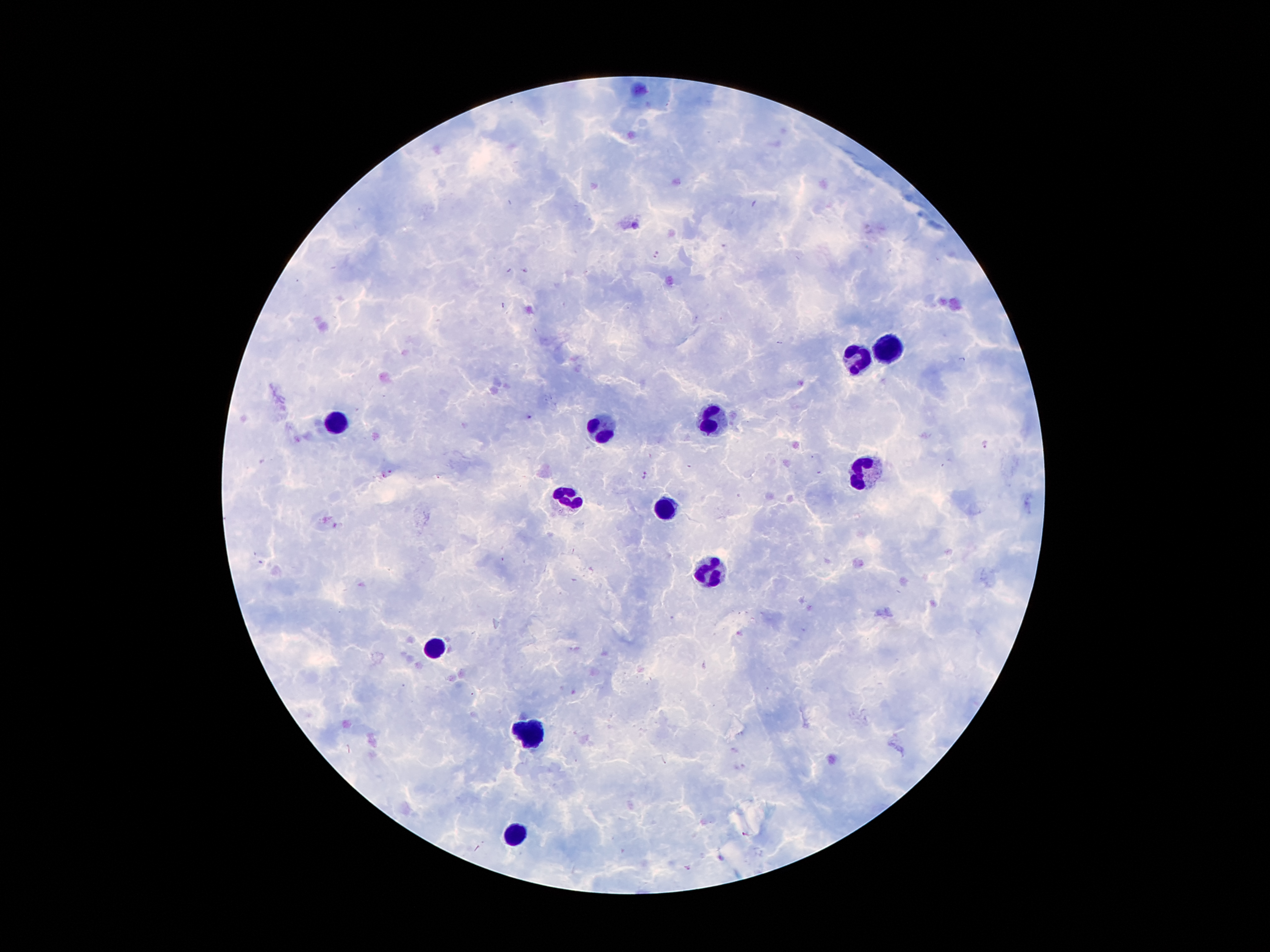
leukocyte_locations: 'approximate object centers, in pixels from the top-left corner: (x=889, y=348), (x=860, y=360), (x=717, y=417), (x=331, y=421), (x=600, y=427), (x=866, y=475), (x=569, y=495), (x=665, y=507), (x=711, y=571), (x=438, y=647), (x=528, y=735), (x=516, y=833)'
malaria_parasite_locations: 'approximate object centers, in pixels from the top-left corner: (x=657, y=255), (x=509, y=270), (x=526, y=270), (x=503, y=305), (x=529, y=416), (x=985, y=445), (x=388, y=471), (x=646, y=475), (x=745, y=834), (x=688, y=867)'
preparation: thick blood film
stain: Giemsa
field_of_view: single
image_size: 1270×952 pixels
patient_malaria_status: positive for Plasmodium falciparum
magnification: 100x
capture: smartphone through the microscope eyepiece